Outline each blood parasite and name the species.
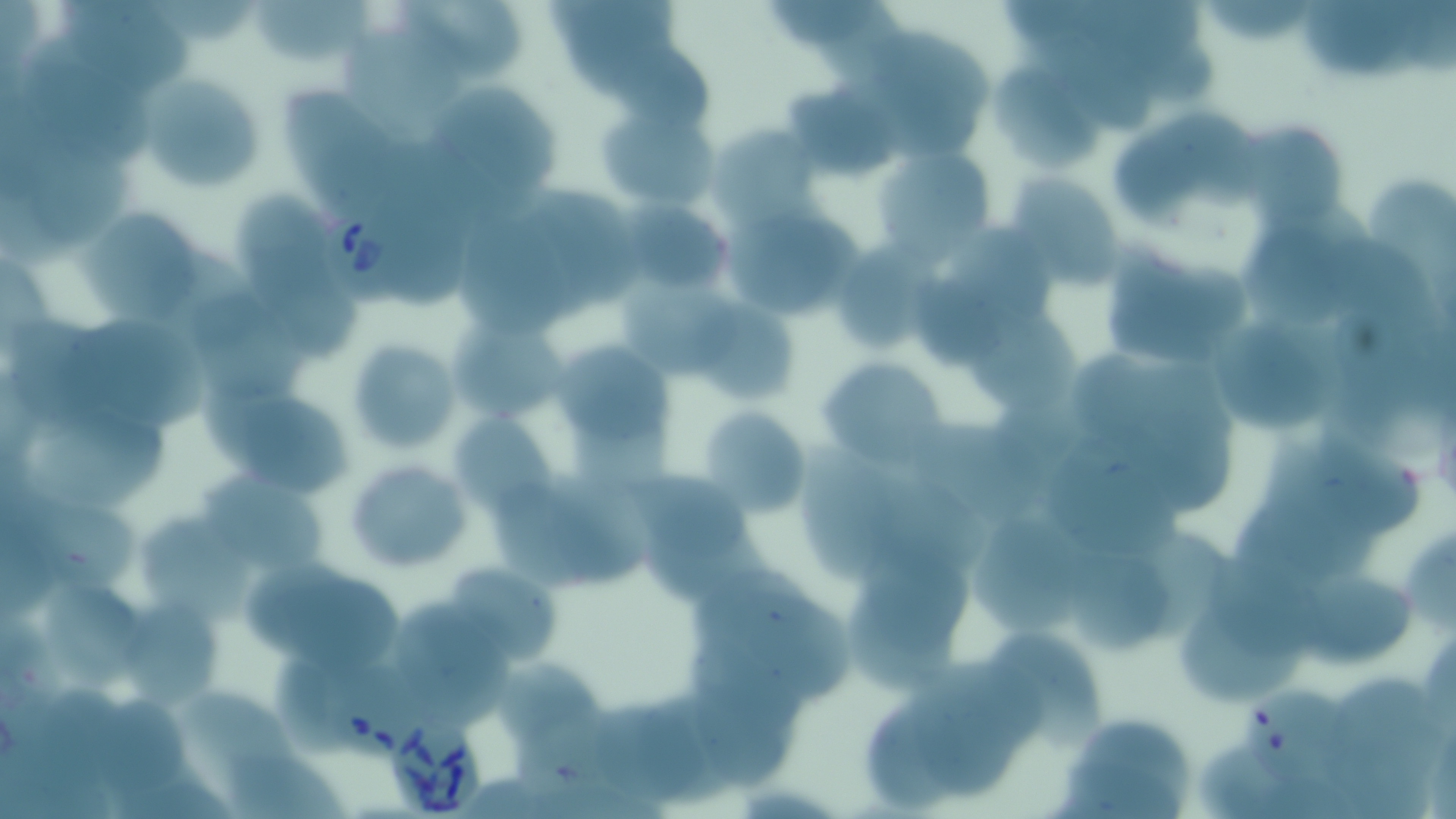

Approximate bounding boxes as (x1, y1, x2, y2) in pixels.
Babesia divergens-infected red blood cells: (321, 197, 420, 307), (328, 660, 426, 762), (393, 720, 489, 813).
No Plasmodium falciparum, Plasmodium ovale, Plasmodium malariae, Plasmodium vivax, or Trypanosoma brucei observed.

Uninfected red blood cell locations: (58, 0, 195, 90), (399, 0, 522, 78), (773, 0, 887, 47), (999, 0, 1090, 42), (1213, 0, 1316, 43), (1307, 0, 1421, 77), (255, 1, 377, 68), (1097, 1, 1206, 63), (816, 6, 919, 88), (20, 24, 154, 161), (344, 29, 468, 145), (865, 30, 1001, 129), (603, 31, 713, 130), (1031, 37, 1154, 133), (1137, 43, 1221, 104), (993, 66, 1105, 172), (145, 72, 266, 192), (432, 75, 560, 196), (785, 75, 904, 173), (279, 90, 405, 206), (597, 95, 719, 213), (1172, 112, 1271, 204), (1234, 117, 1348, 225), (711, 120, 821, 225), (1120, 120, 1204, 212), (28, 130, 136, 236), (877, 139, 998, 260), (1366, 170, 1456, 295), (1006, 175, 1126, 287), (377, 186, 474, 309), (532, 186, 645, 309), (231, 189, 329, 294), (75, 201, 209, 328), (626, 202, 730, 297), (722, 205, 863, 322), (454, 207, 577, 337), (1245, 224, 1354, 324), (838, 232, 951, 352), (1329, 233, 1439, 330), (147, 247, 265, 353), (1095, 247, 1252, 370), (0, 254, 56, 357), (270, 287, 360, 359), (193, 293, 309, 399), (696, 297, 799, 400), (970, 304, 1080, 412), (439, 309, 563, 427), (72, 318, 223, 428), (9, 320, 117, 426), (1210, 320, 1335, 427), (345, 338, 461, 453), (549, 342, 672, 456), (1070, 351, 1167, 444), (819, 358, 947, 468), (220, 387, 356, 502), (445, 405, 568, 522), (697, 406, 813, 517), (29, 408, 170, 511), (1134, 412, 1238, 511), (903, 421, 1050, 509), (1317, 424, 1428, 532), (1045, 426, 1188, 568), (803, 442, 905, 586), (1271, 442, 1382, 577), (341, 457, 476, 575), (612, 467, 752, 563), (867, 467, 992, 581), (192, 471, 329, 578), (543, 471, 655, 583), (493, 485, 595, 588), (1233, 487, 1336, 594), (33, 489, 143, 602), (144, 510, 268, 629), (965, 510, 1091, 643), (644, 525, 770, 606), (1126, 525, 1226, 639), (855, 535, 968, 650), (1410, 540, 1456, 636), (1067, 551, 1178, 659), (1211, 558, 1337, 654), (439, 561, 558, 670), (245, 565, 407, 667), (697, 571, 827, 668), (1311, 575, 1418, 669), (46, 588, 150, 694), (844, 591, 968, 688), (1177, 595, 1316, 707), (749, 596, 855, 702), (130, 601, 226, 707), (401, 601, 512, 727), (990, 629, 1111, 741), (275, 660, 357, 757), (497, 662, 613, 748), (910, 663, 1019, 802), (1331, 674, 1440, 765), (693, 686, 787, 786), (190, 687, 303, 772), (1244, 690, 1351, 787), (865, 694, 954, 813), (106, 703, 189, 797), (593, 703, 712, 805), (520, 710, 633, 796), (1054, 710, 1199, 819), (1196, 736, 1292, 815), (1327, 741, 1434, 819), (225, 750, 353, 819), (115, 767, 230, 819), (1265, 772, 1363, 819). Slide-level diagnosis: Babesia divergens. Optical microscopy. Thin blood film. Image is 1456×819 pixels. May-Grünwald-Giemsa-stained preparation. One field of a larger specimen. 1000x magnification.